Report the malaria status of this cell.
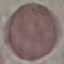

Uninfected.

Summary:
  - Stain: Giemsa
  - Image type: automatically extracted cell patch, resized to 64 × 64 pixels
  - Capture: smartphone through the microscope eyepiece
  - Preparation: thin blood film